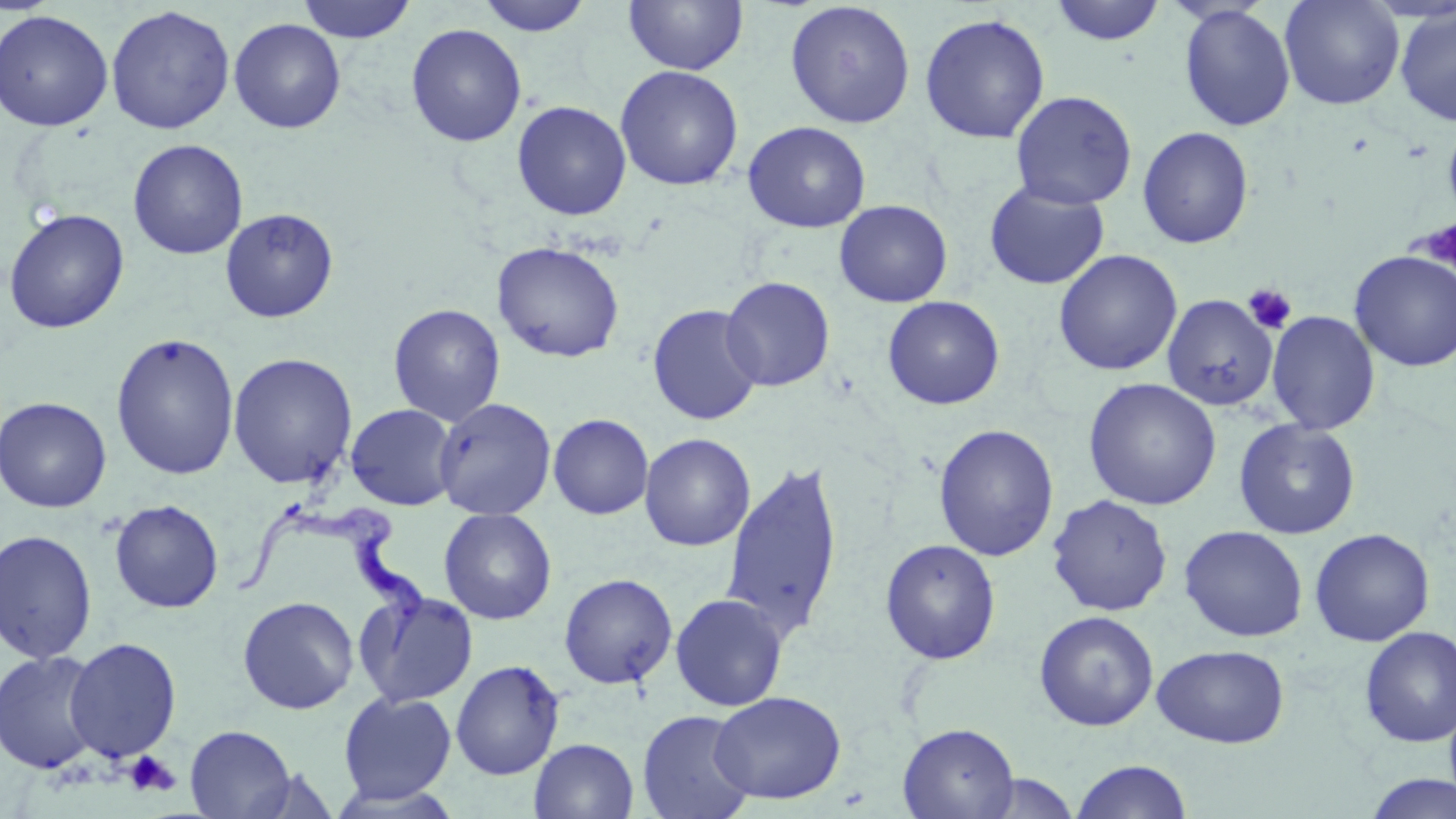 Approximate bounding boxes as [x1, y1, x2, y2] in pixels. Platelet locations: [1421, 219, 1455, 278], [1242, 283, 1298, 335], [123, 751, 181, 797]. Uninfected red blood cell locations: [296, 0, 418, 44], [475, 0, 594, 37], [623, 0, 749, 75], [1049, 0, 1167, 46], [1279, 0, 1405, 110], [784, 1, 916, 129], [105, 5, 236, 135], [1178, 5, 1296, 131], [1395, 6, 1456, 126], [0, 9, 114, 131], [919, 12, 1051, 144], [228, 18, 346, 134], [406, 23, 527, 147], [615, 65, 744, 191], [1010, 90, 1137, 210], [512, 100, 631, 221], [1442, 119, 1456, 224], [743, 121, 871, 233], [1137, 126, 1254, 249], [128, 139, 248, 260], [984, 181, 1110, 290], [834, 200, 953, 307], [220, 207, 339, 323], [3, 208, 130, 334], [492, 241, 625, 363], [1053, 249, 1182, 376], [1349, 250, 1456, 372], [720, 276, 835, 392], [1161, 294, 1279, 411], [882, 296, 1005, 410], [388, 303, 505, 426], [647, 304, 763, 426], [1266, 310, 1380, 435], [111, 332, 240, 480], [227, 352, 358, 489], [1083, 377, 1221, 510], [0, 396, 112, 513], [434, 397, 556, 521], [345, 403, 459, 511], [548, 414, 653, 519], [1233, 418, 1361, 539], [933, 424, 1059, 562], [639, 433, 756, 551], [720, 460, 844, 641], [1047, 495, 1173, 616], [109, 499, 224, 613], [438, 507, 557, 625], [1179, 525, 1308, 642], [1309, 528, 1435, 647], [0, 529, 98, 664], [880, 538, 1001, 664], [558, 573, 678, 689], [353, 588, 479, 708], [670, 593, 788, 711], [237, 596, 359, 714], [1033, 610, 1159, 731], [1358, 626, 1456, 747], [64, 637, 182, 763], [1152, 644, 1289, 748], [0, 651, 104, 774], [450, 659, 564, 780], [338, 691, 457, 805], [710, 691, 846, 804], [637, 710, 755, 819], [898, 723, 1019, 819], [184, 724, 296, 818], [529, 738, 639, 819], [1070, 759, 1193, 818], [973, 773, 1081, 818], [1361, 773, 1456, 818]. Trypanosoma brucei locations: [236, 505, 428, 657]. Slide-level diagnosis: Trypanosoma brucei. 1000x magnification. Optical microscopy. May-Grünwald-Giemsa stain. Image is 1456×819 pixels. Single field of view. Thin blood smear.